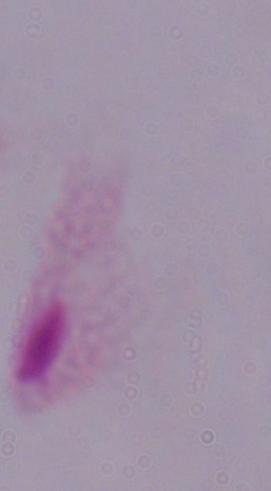
Captured at 1000x magnification. A trichomonad is seen. Photomicrograph.